Report the malaria status of this cell.
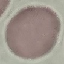

It is uninfected.

Thin smear of blood. Giemsa stain. Cell patch, automatically extracted from a larger field of view and resized to 64 × 64 pixels. Photographed with a smartphone camera at the microscope eyepiece.